Describe the morphology of the erythrocytes.
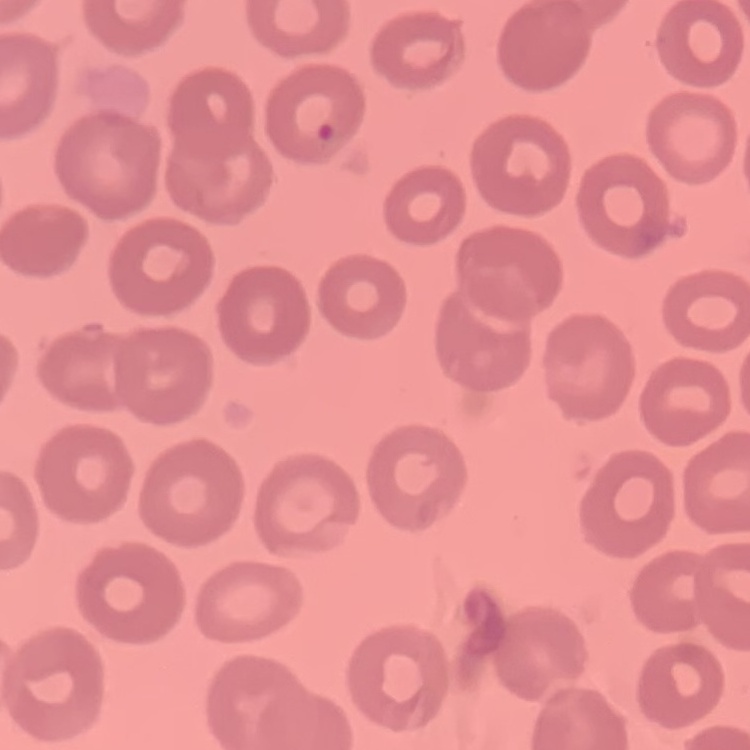

No rouleaux formation.

Thin blood film. Stained with either Field's or Giemsa. Square crop of a larger photomicrograph.